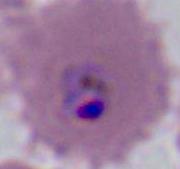
A Plasmodium parasite is seen. Captured at either 400x or 1000x magnification. Micrograph.